Identify the parasite.
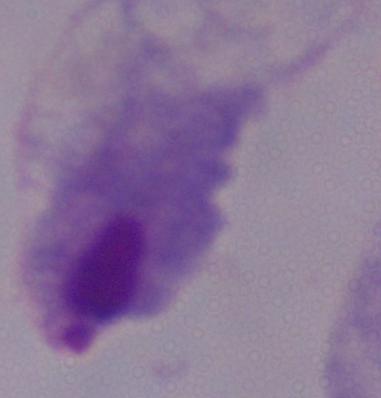

A trichomonad.

modality: photomicrograph
magnification: 1000x